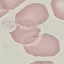

Summary:
  - Result: no malaria parasites seen
  - Image type: cell patch, automatically extracted from a larger field of view and resized to 64 × 64 pixels
  - Capture: smartphone through the microscope eyepiece
  - Preparation: thin blood film
  - Stain: Giemsa